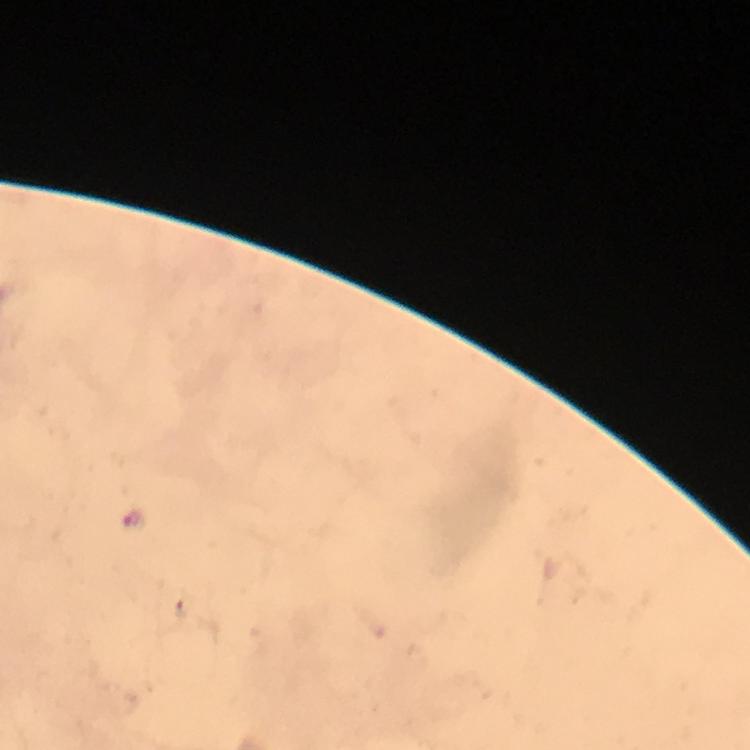

Approximate centers as [x, y] in pixels. Malaria parasite locations: [134, 519]. Smartphone photograph taken through a microscope. From a malaria diagnostic workup. At 100x magnification. Thick smear. Cropped region of a single field of view. Giemsa-stained preparation. Immersion oil was used. Image is 750×750 pixels.